Assess this cell for malaria.
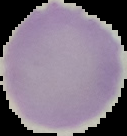
Uninfected.

Summary:
  - Preparation: thin blood film
  - Image size: 127×136 pixels
  - Image type: segmented cell region on a black background